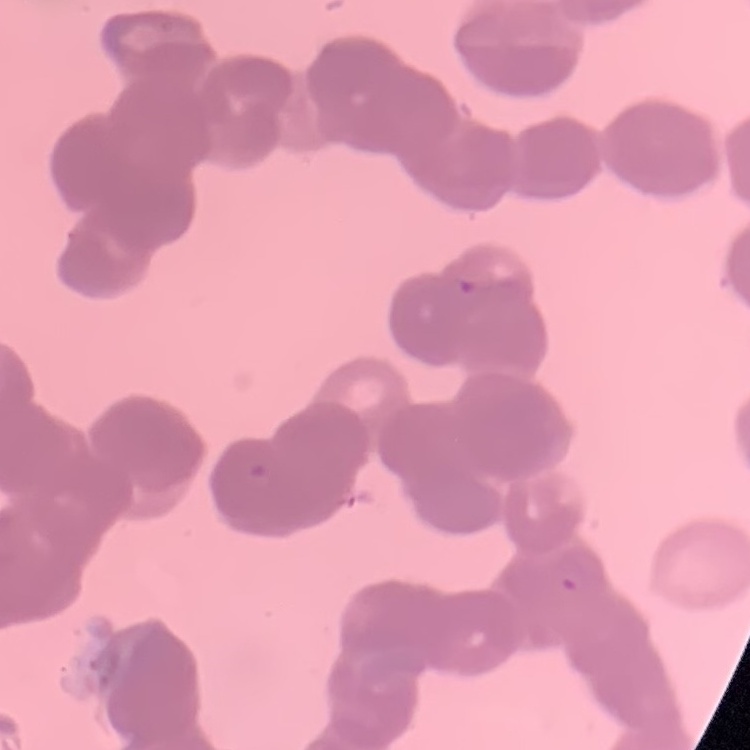
The red blood cells show rouleaux formation. One tile cut from a larger photomicrograph. Field's or Giemsa stain. Thin blood film.